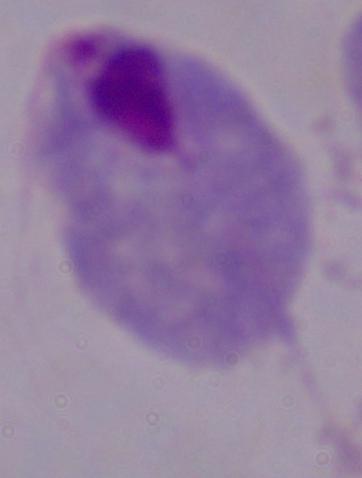

Summary:
  - Modality: photomicrograph
  - Magnification: 1000x
  - Identification: trichomonad